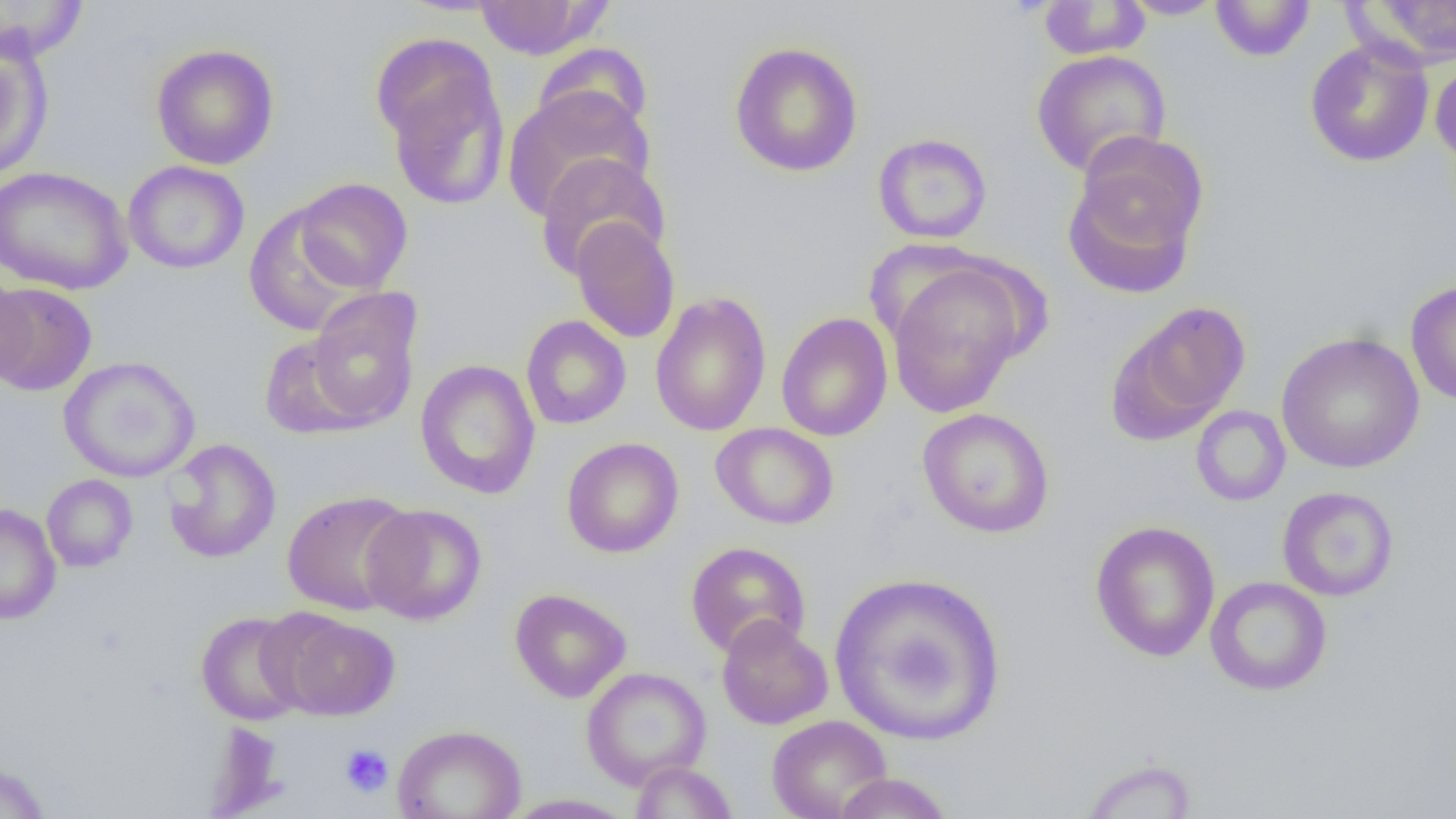
slide-level diagnosis = negative for blood parasites
image size = 1456×819 pixels
uninfected red blood cell locations = approximate bounding boxes as (x1, y1, x2, y2) in pixels: (1, 0, 89, 63), (1119, 0, 1226, 20), (1210, 0, 1315, 61), (474, 1, 606, 59), (1037, 1, 1150, 60), (1350, 1, 1456, 69), (371, 31, 498, 144), (0, 38, 53, 179), (1305, 40, 1434, 167), (729, 41, 864, 177), (532, 42, 654, 143), (151, 43, 279, 170), (1031, 49, 1171, 178), (383, 56, 510, 211), (1430, 57, 1456, 172), (502, 86, 653, 222), (873, 133, 992, 244), (1063, 142, 1204, 300), (535, 153, 670, 280), (122, 160, 250, 275), (0, 166, 134, 295), (292, 178, 413, 293), (244, 204, 364, 337), (570, 218, 680, 343), (887, 261, 1029, 418), (1, 270, 35, 390), (1405, 279, 1456, 406), (0, 282, 98, 396), (305, 288, 423, 430), (650, 292, 772, 437), (1109, 302, 1251, 442), (776, 312, 893, 442), (521, 315, 631, 430), (1276, 332, 1425, 473), (259, 334, 370, 440), (59, 356, 200, 483), (415, 359, 540, 500), (1190, 405, 1290, 506), (917, 407, 1055, 538), (711, 422, 839, 530), (561, 437, 684, 558), (163, 438, 281, 563), (42, 474, 138, 572), (1277, 486, 1399, 602), (281, 490, 416, 616), (0, 503, 61, 625), (360, 503, 487, 625), (1090, 520, 1220, 662), (685, 541, 811, 658), (828, 572, 1007, 745), (1205, 576, 1332, 696), (509, 588, 632, 702), (195, 611, 309, 725), (272, 612, 401, 721), (716, 615, 832, 729), (581, 667, 711, 789), (767, 714, 893, 819), (392, 724, 527, 819), (1078, 757, 1199, 819), (0, 759, 51, 819), (630, 760, 738, 818), (831, 773, 956, 818), (503, 793, 636, 818)
magnification = 1000x
modality = light microscopy
field of view = one of a larger specimen
preparation = thin blood smear
platelet locations = approximate bounding boxes as (x1, y1, x2, y2) in pixels: (340, 744, 394, 798)